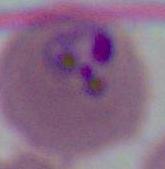

modality: photomicrograph
magnification: 400x or 1000x
identification: Plasmodium